State which parasite is depicted.
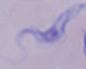
A trypanosome.

Micrograph. 1000x magnification.